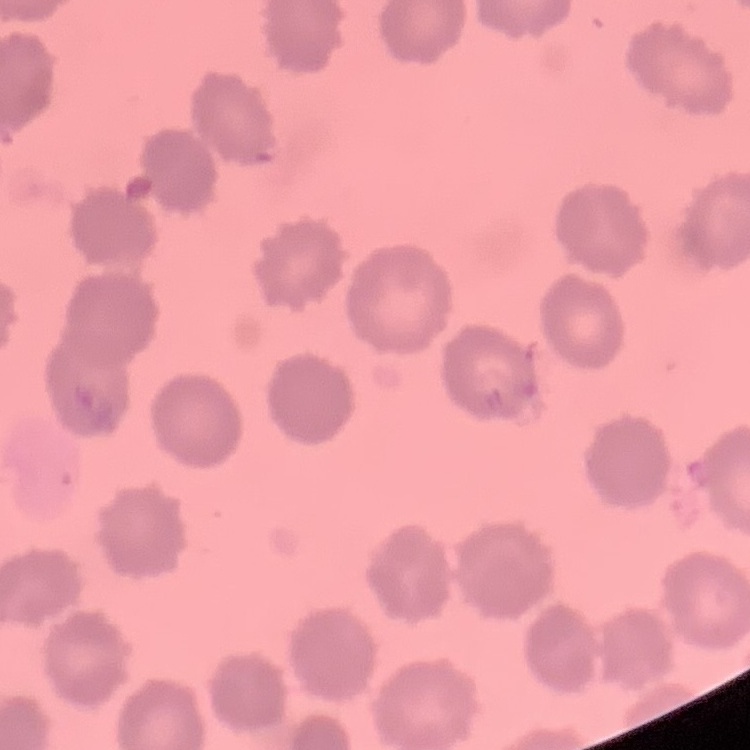 The erythrocytes exhibit no rouleaux formation. Field's or Giemsa stain. Square crop of a larger photomicrograph. Thin blood film.